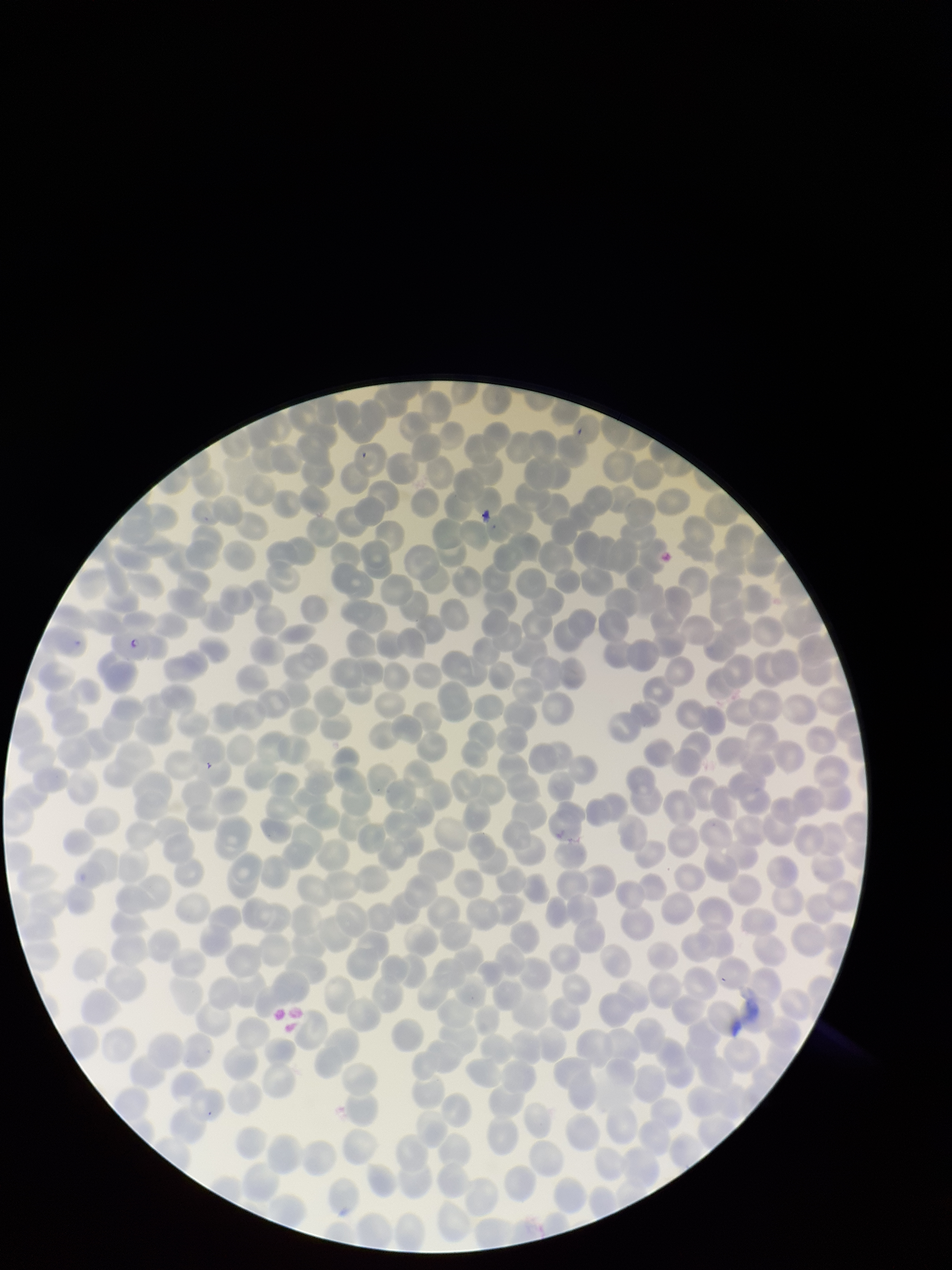

{
  "preparation": "thin",
  "red_blood_cell_count": 262,
  "field_of_view": "single",
  "image_size": "952×1270 pixels",
  "capture": "smartphone photograph through the microscope eyepiece",
  "parasitized_red_blood_cell_count": 0,
  "parasitized_red_blood_cells": "none identified",
  "species_reported_for_this_patient": "Plasmodium falciparum",
  "patient_malaria_status": "positive",
  "stain": "Giemsa"
}